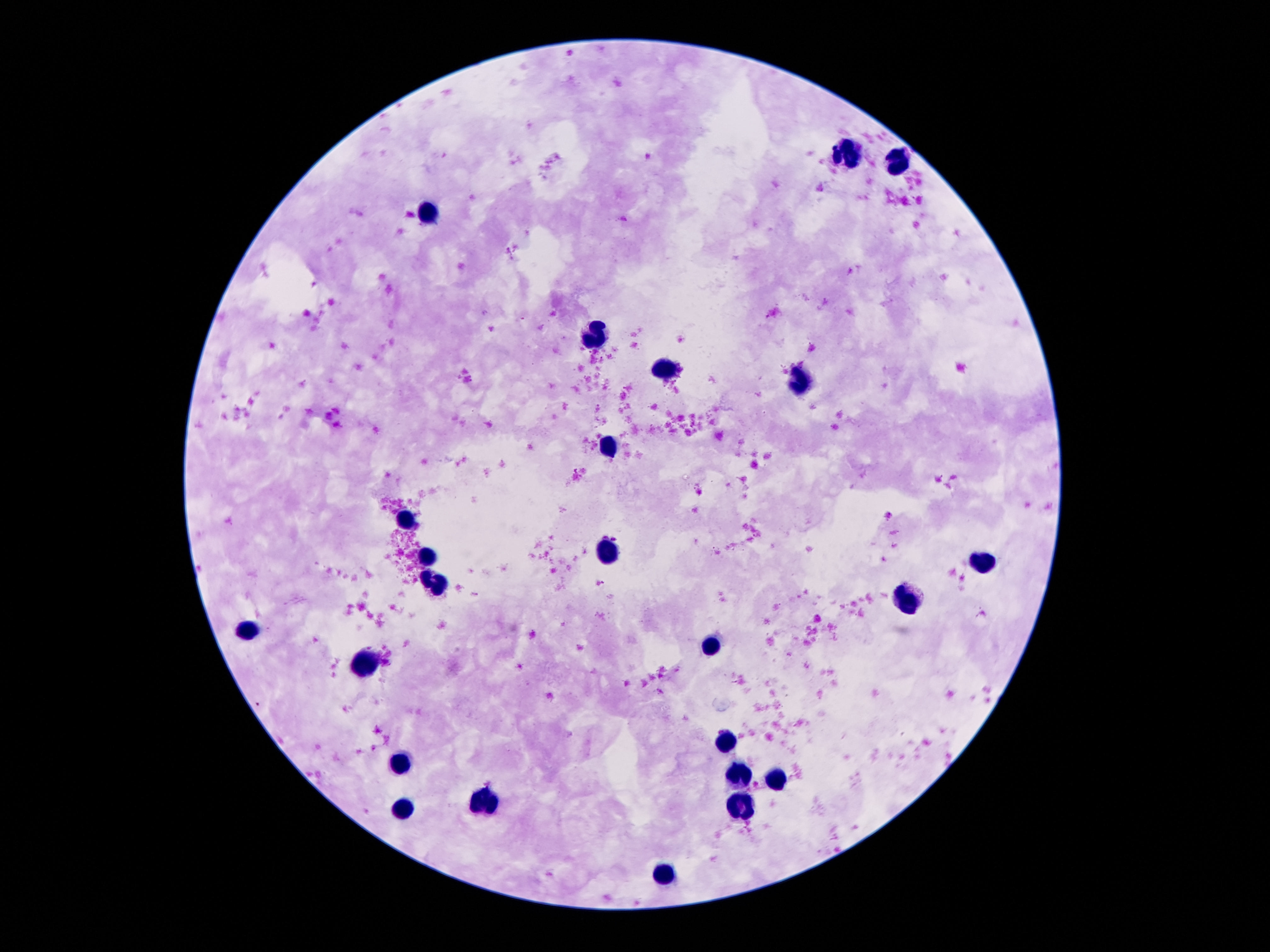
field of view = single
patient malaria status = negative
magnification = 100x
preparation = thick blood smear
image size = 1270×952 pixels
stain = Giemsa
capture = smartphone camera through the microscope eyepiece
leukocyte locations = approximate object centers, in pixels from the top-left corner: (x=846, y=155), (x=893, y=163), (x=430, y=211), (x=594, y=336), (x=671, y=373), (x=800, y=383), (x=610, y=445), (x=405, y=516), (x=608, y=549), (x=426, y=553), (x=983, y=562), (x=436, y=584), (x=907, y=600), (x=245, y=631), (x=712, y=648), (x=366, y=666), (x=725, y=738), (x=399, y=770), (x=739, y=775), (x=778, y=782), (x=485, y=802), (x=739, y=805), (x=403, y=812), (x=663, y=879)